Report the malaria status of this cell.
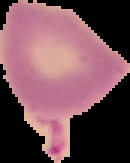
It is uninfected.

{
  "preparation": "thin blood smear",
  "image_size": "130×163 pixels",
  "image_type": "segmented cell region on a black background"
}